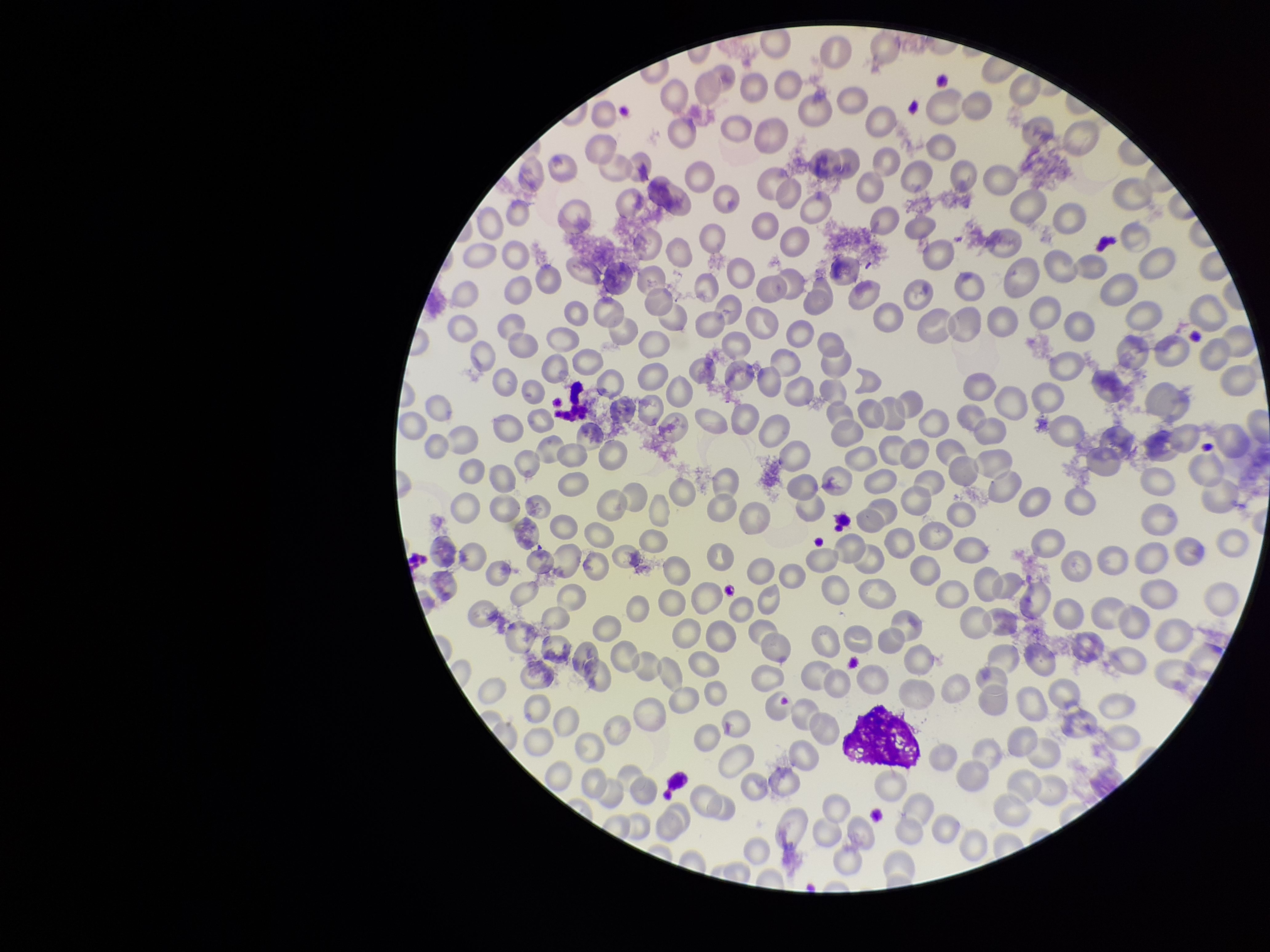

Summary:
  - Red blood cell count: 237
  - Capture: smartphone photograph through the microscope eyepiece
  - Patient malaria status: negative
  - Parasitized red blood cell count: 0
  - Parasitized red blood cells: none identified
  - Preparation: thin blood smear
  - Stain: Giemsa
  - Field of view: one from this slide
  - Image size: 1270×952 pixels